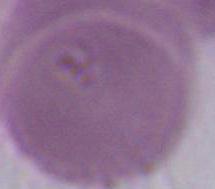 Captured at 1000x magnification. Micrograph. A red blood cell is seen.